Identify the parasite.
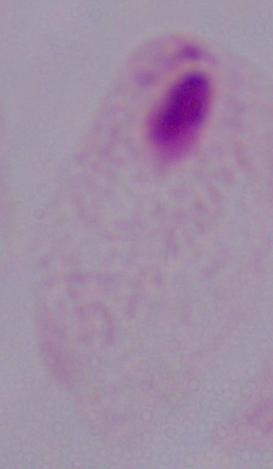
This is a trichomonad.

Summary:
  - Magnification: 1000x
  - Modality: micrograph